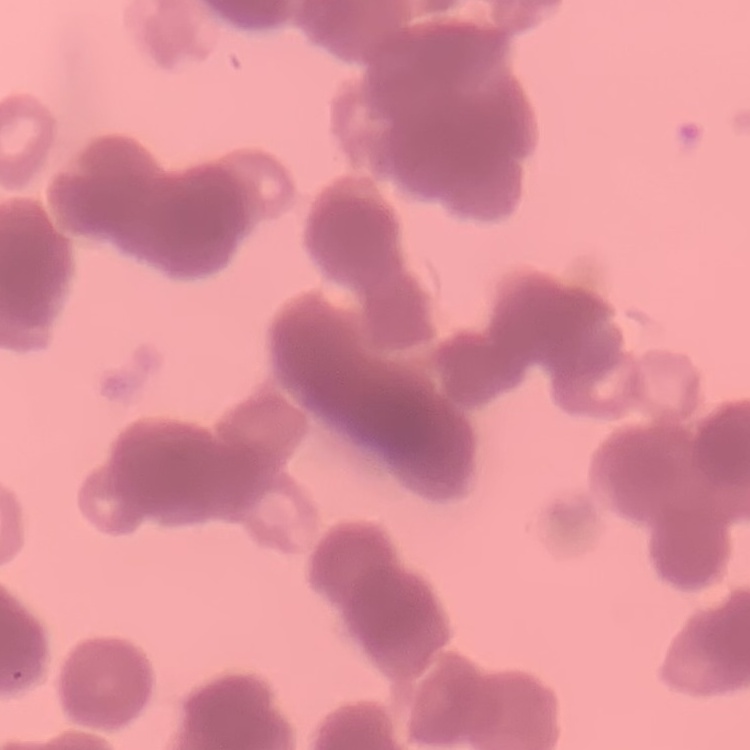

Summary:
  - Red blood cell morphology: rouleaux formation
  - Preparation: thin blood film
  - Image type: square crop of a larger photomicrograph
  - Stain: Field's or Giemsa